Locate and identify every blood parasite.
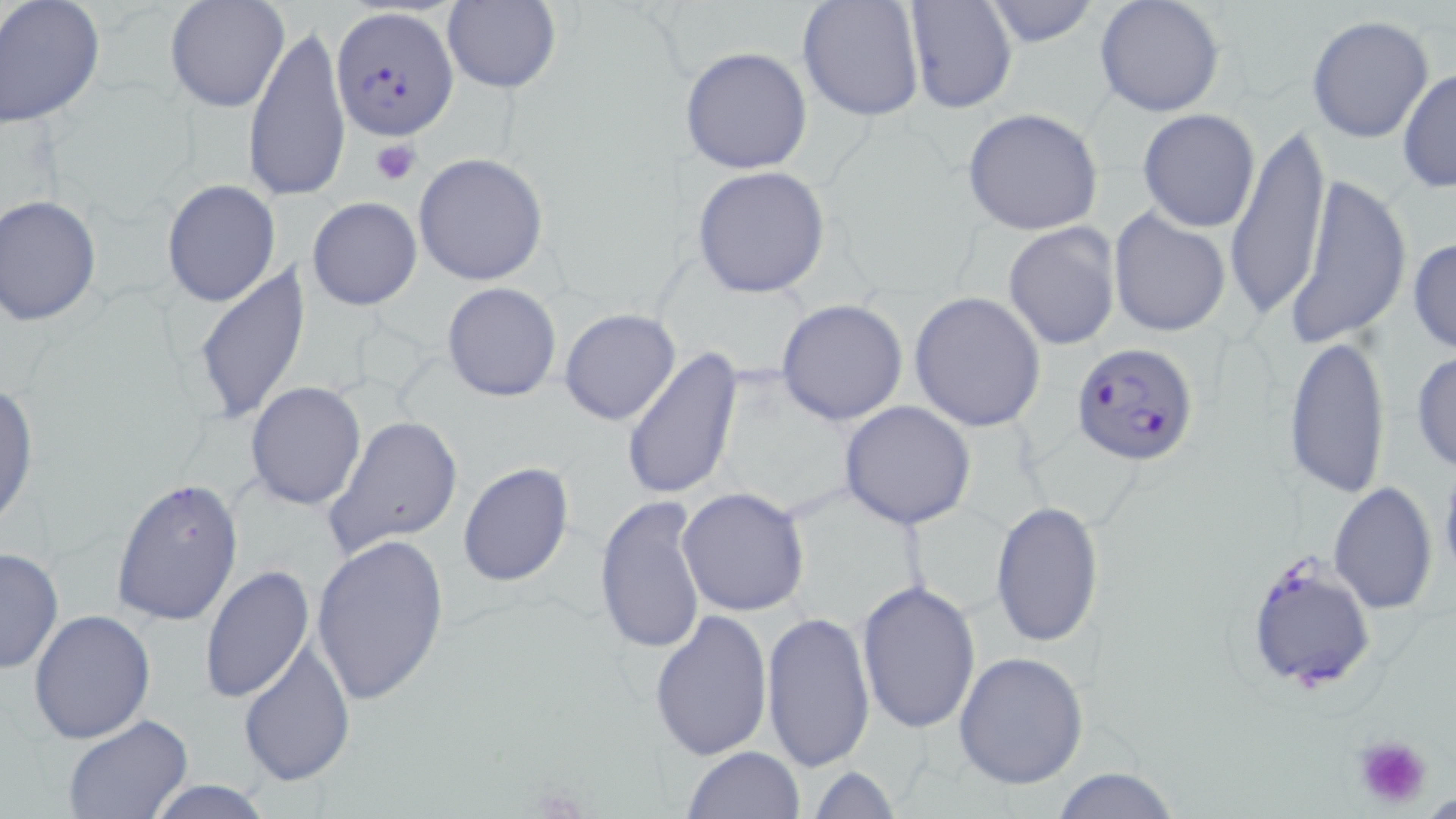

Approximate bounding boxes as (x1,y1)-(x2,y2) corner pairs in pixels.
Plasmodium falciparum-infected red blood cells: (328,5)-(458,141), (1072,342)-(1201,466), (1244,549)-(1378,693).
No Plasmodium ovale, Plasmodium malariae, Plasmodium vivax, Babesia divergens, or Trypanosoma brucei observed.

Platelet locations: (371,139)-(422,185), (1351,734)-(1434,808). Uninfected red blood cell locations: (164,0)-(289,113), (797,0)-(925,123), (903,0)-(1018,115), (979,0)-(1100,48), (1095,0)-(1225,118), (0,1)-(106,129), (442,1)-(561,94), (1307,16)-(1433,142), (244,21)-(351,206), (680,46)-(813,175), (1398,68)-(1455,193), (961,108)-(1103,236), (1138,109)-(1261,232), (1225,119)-(1332,321), (414,153)-(548,285), (692,166)-(832,298), (1283,171)-(1411,352), (162,179)-(281,308), (0,196)-(102,325), (307,198)-(421,311), (1108,208)-(1233,338), (1003,222)-(1122,350), (1408,235)-(1456,356), (191,262)-(311,426), (442,282)-(561,402), (909,292)-(1045,431), (775,298)-(909,426), (560,310)-(681,426), (1283,335)-(1391,500), (623,346)-(743,502), (1411,350)-(1456,475), (245,381)-(366,510), (1,383)-(37,530), (839,402)-(976,530), (324,414)-(465,559), (1440,453)-(1456,587), (456,460)-(575,588), (111,477)-(243,625), (1329,480)-(1438,615), (677,489)-(809,616), (594,494)-(709,656), (989,501)-(1104,650), (310,533)-(450,707), (0,546)-(64,674), (201,565)-(314,705), (857,579)-(981,735), (29,608)-(157,744), (649,608)-(774,761), (760,611)-(875,775), (237,637)-(356,789), (953,650)-(1089,790), (61,715)-(191,819), (682,746)-(803,819), (807,765)-(901,819), (1044,767)-(1186,819), (141,779)-(276,818). Slide-level diagnosis: Plasmodium falciparum. One field of a larger specimen. Image is 1456×819 pixels. May-Grünwald-Giemsa stain. Light microscopy. Captured at 1000x magnification. Thin blood smear.